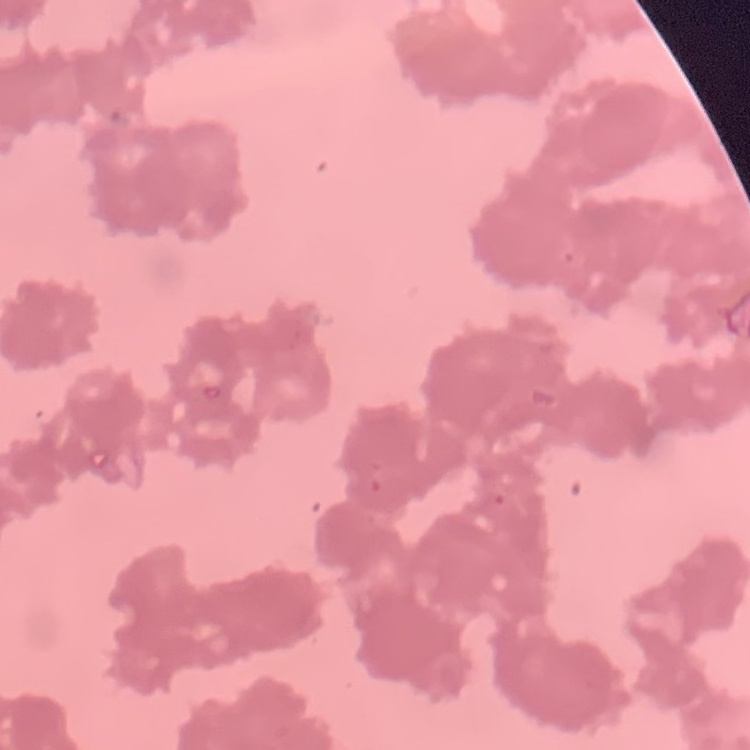
The erythrocytes exhibit rouleaux formation. Thin peripheral smear. Field's or Giemsa stain. Square crop of a larger photomicrograph.